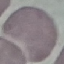
malaria status = uninfected
stain = Giemsa
image type = cell patch, automatically extracted from a larger field of view and resized to 64 × 64 pixels
capture = smartphone through the microscope eyepiece
preparation = thin blood film